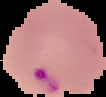
Summary:
  - Preparation: thin blood smear
  - Image size: 106×97 pixels
  - Malaria status: parasitized
  - Image type: segmented cell region on a black background